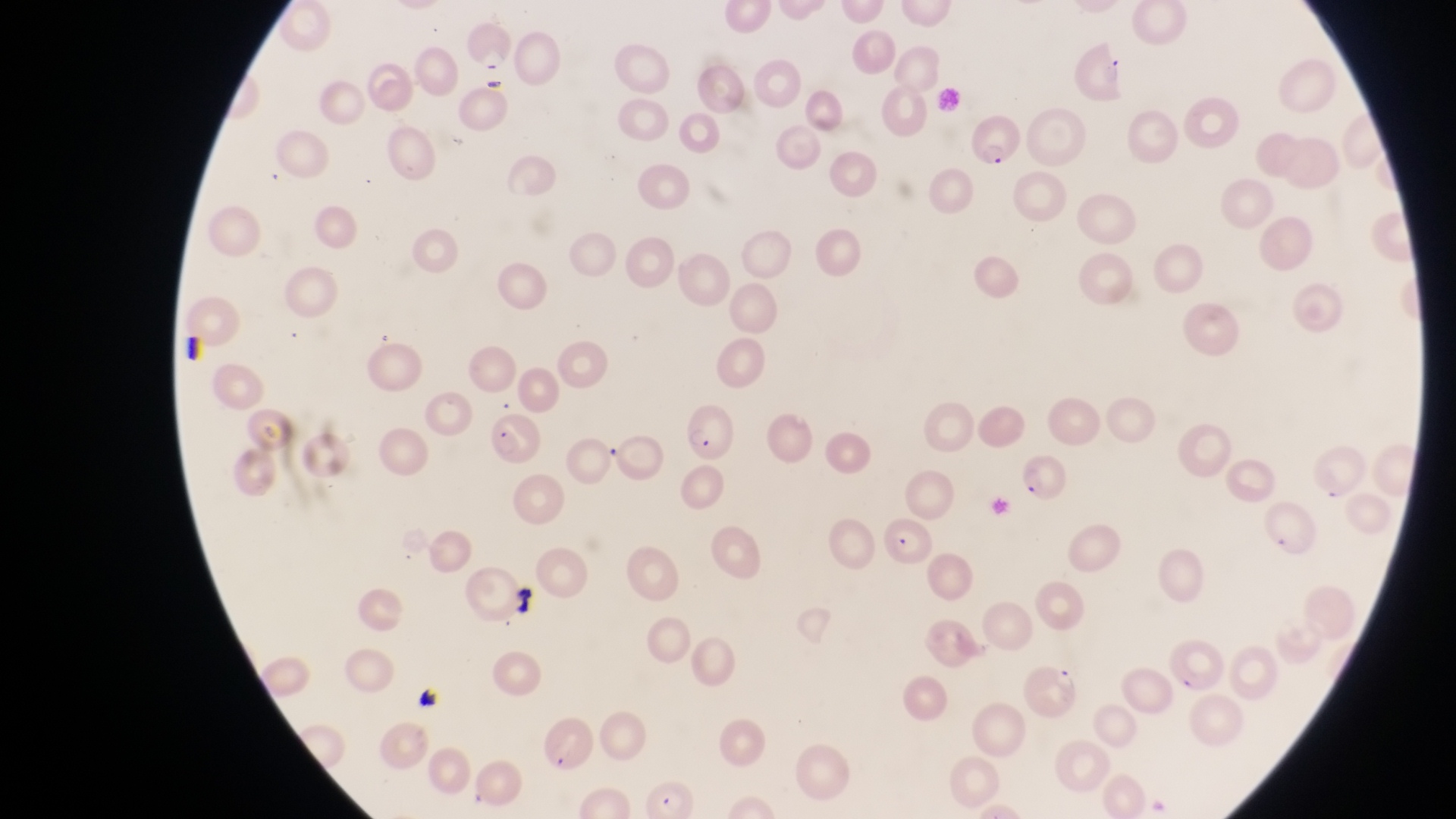
Approximate bounding boxes as {left, top, right, bottom} in pixels.
Summary:
  - Artifact (platelet-like body, stain precipitate, or debris) locations: {510, 584, 540, 620}, {412, 686, 445, 717}
  - Parasitised red blood cell locations: {965, 115, 1018, 168}, {680, 406, 736, 458}, {486, 410, 545, 462}, {1305, 442, 1372, 503}, {1012, 455, 1065, 504}, {885, 516, 937, 571}, {1027, 661, 1082, 724}, {536, 717, 591, 772}
  - Preparation: thin blood film
  - Country: Uganda
  - Image size: 1456×819 pixels
  - Field of view: single
  - Magnification: 1000x
  - Capture: smartphone photograph through the eyepiece of an Olympus CX-23 microscope